Classify this cell by malaria status.
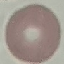

It is uninfected.

Automatically extracted cell patch, resized to 64 × 64 pixels. Giemsa stain. Thin blood smear. Acquired by smartphone through the microscope eyepiece.